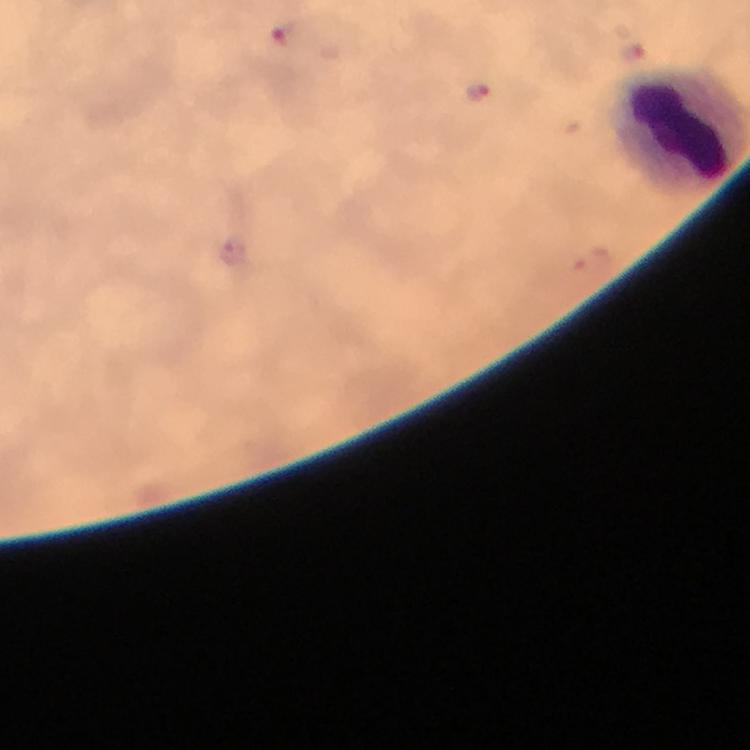

context: from a malaria diagnostic workup
preparation: thick blood film
cropped_from: a single field of view
image_size: 750×750 pixels
malaria_parasite_locations: 'approximate centers as [x, y] in pixels: [288, 37], [476, 90], [231, 253]'
stain: Giemsa
magnification: 100x
immersion_oil: applied
capture: smartphone mounted on the microscope